Assess the morphology of the red blood cells.
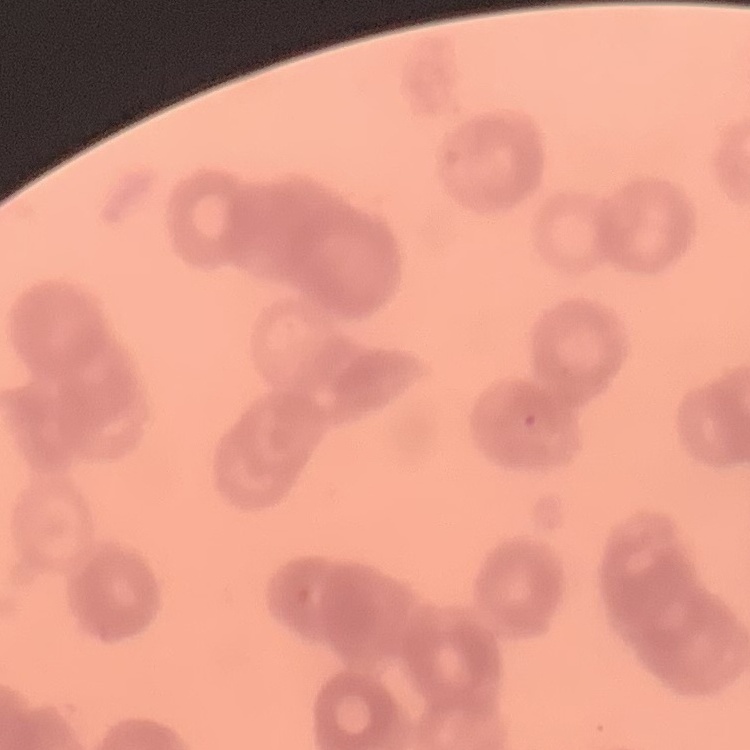
Rouleaux formation.

Summary:
  - Image type: square crop of a larger photomicrograph
  - Stain: Field's or Giemsa
  - Preparation: thin peripheral smear